Identify the parasite.
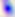
This is Toxoplasma gondii.

400x magnification. Photomicrograph.